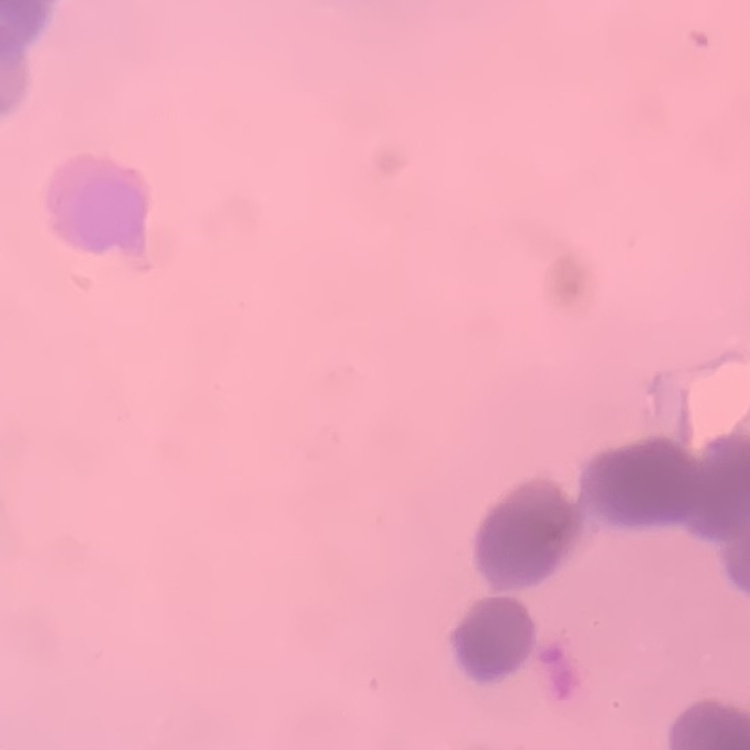
{
  "erythrocyte_morphology": "rouleaux formation",
  "stain": "Field's or Giemsa",
  "preparation": "thin peripheral smear",
  "image_type": "square crop of a larger photomicrograph"
}